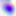

modality: photomicrograph
identification: Toxoplasma gondii
magnification: 400x